State which parasite is depicted.
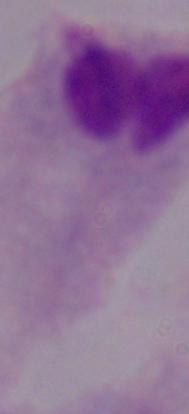
This is a trichomonad.

Photomicrograph. Captured at 1000x magnification.